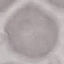
malaria status = uninfected
preparation = thin blood smear
image type = cell patch, automatically extracted from a larger field of view and resized to 64 × 64 pixels
stain = Giemsa
capture = smartphone camera at the microscope eyepiece